Comment on the morphology of the red blood cells.
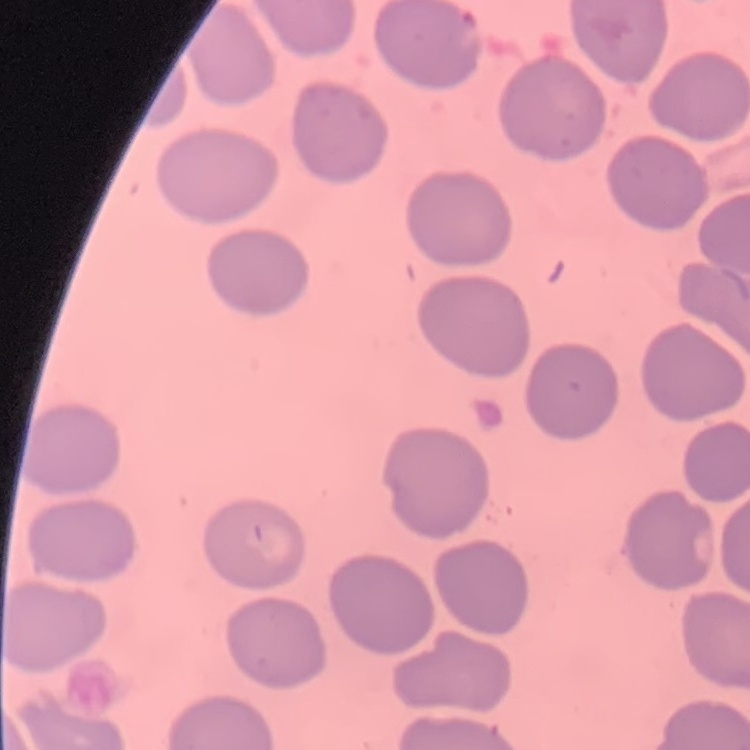
They show no rouleaux formation.

Summary:
  - Preparation: thin blood smear
  - Image type: one tile cut from a larger photomicrograph
  - Stain: Field's or Giemsa